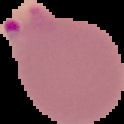

Summary:
  - Preparation: thin blood film
  - Result: malaria parasites detected
  - Image size: 124×124 pixels
  - Image type: segmented cell region with the area outside set to black